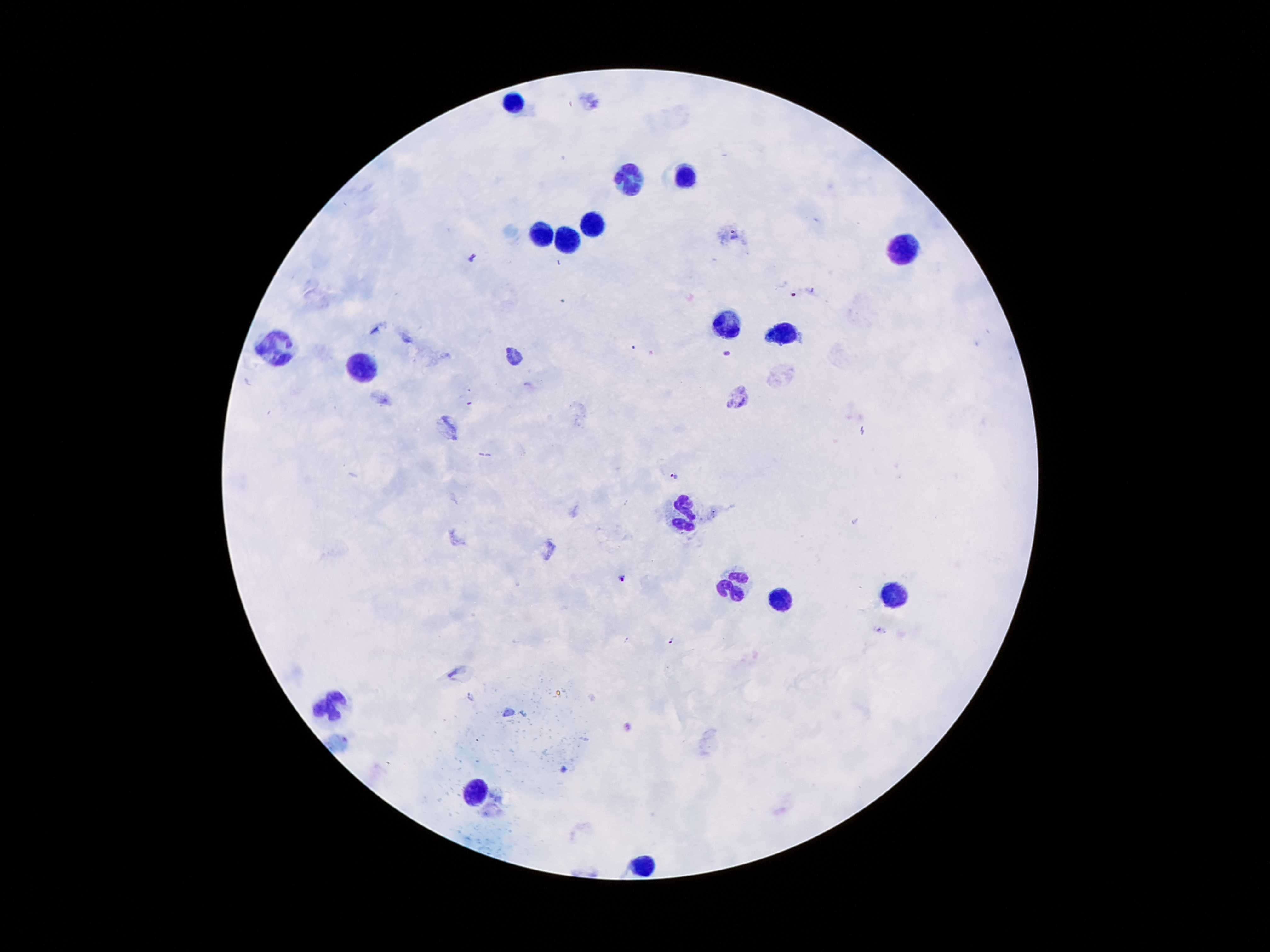

Approximate object centers, in pixels from the top-left corner. Leukocyte locations: (x=511, y=104), (x=685, y=176), (x=627, y=184), (x=594, y=226), (x=538, y=234), (x=569, y=243), (x=902, y=248), (x=725, y=326), (x=783, y=334), (x=277, y=349), (x=361, y=372), (x=683, y=514), (x=734, y=586), (x=891, y=594), (x=777, y=601), (x=331, y=705), (x=476, y=797), (x=646, y=867). Plasmodium parasite locations: (x=733, y=237), (x=474, y=258), (x=726, y=353), (x=673, y=476), (x=621, y=578), (x=673, y=641). Giemsa-stained preparation. Patient malaria status: infected with Plasmodium falciparum. Thick blood smear. Image is 1270×952 pixels. 100x magnification. Single field of view. Photographed through the microscope eyepiece with a smartphone camera.